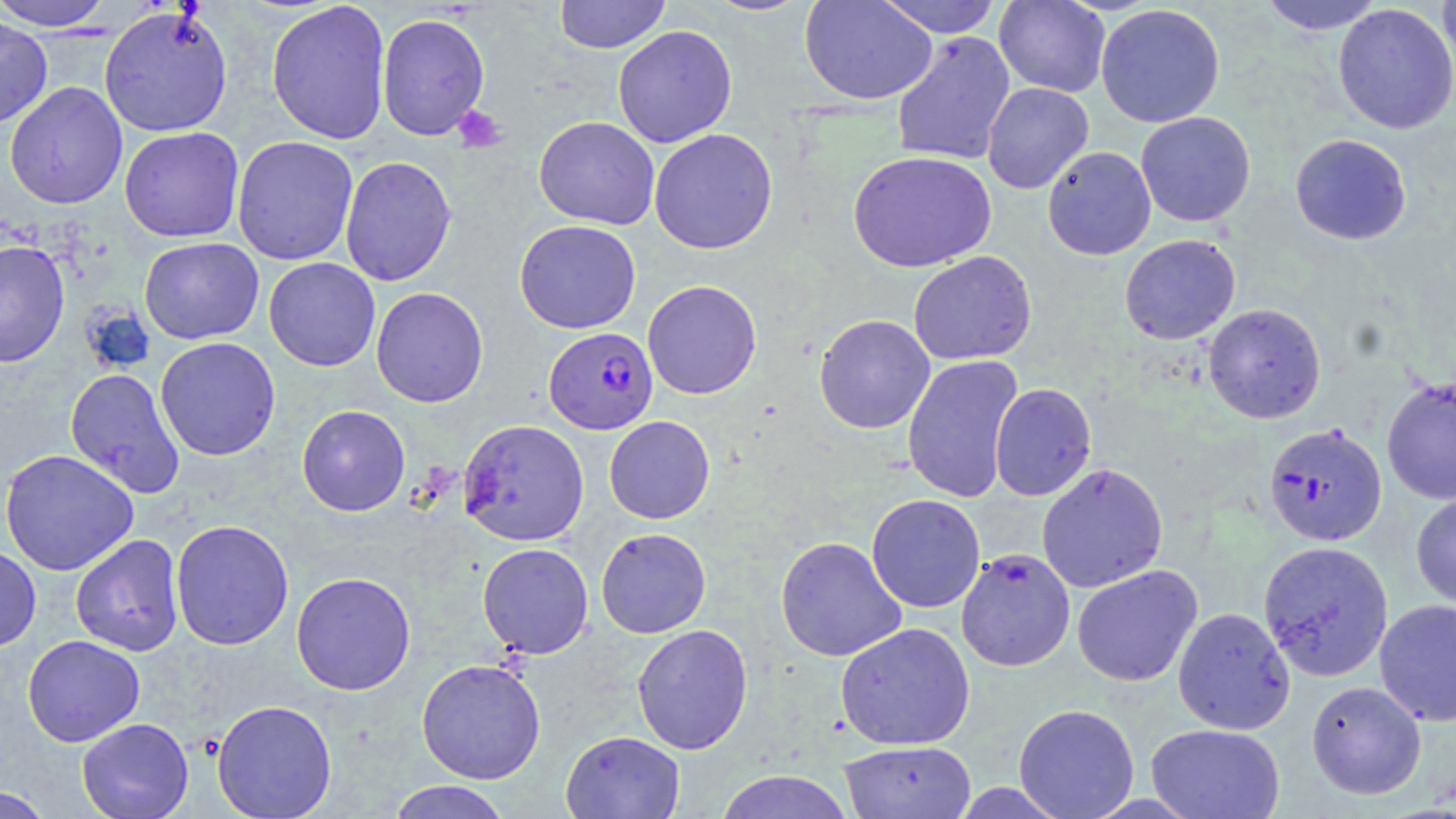

Summary:
  - Coordinate format: approximate bounding boxes as (x1, y1, x2, y2) in pixels
  - Uninfected red blood cell locations: (0, 0, 117, 31), (554, 0, 671, 54), (702, 0, 813, 17), (799, 0, 937, 105), (875, 0, 1003, 38), (994, 0, 1110, 97), (1257, 0, 1388, 35), (1437, 0, 1456, 83), (266, 1, 391, 144), (1333, 3, 1456, 135), (1096, 4, 1225, 128), (98, 5, 234, 138), (377, 12, 490, 141), (0, 15, 53, 129), (613, 24, 738, 148), (891, 31, 1016, 166), (4, 82, 128, 210), (982, 82, 1093, 194), (1136, 111, 1256, 227), (534, 116, 659, 230), (119, 127, 244, 242), (649, 128, 778, 254), (1290, 133, 1412, 245), (232, 135, 359, 266), (1042, 146, 1156, 260), (848, 151, 997, 272), (340, 155, 457, 287), (514, 220, 641, 334), (1119, 234, 1240, 344), (139, 237, 264, 344), (0, 240, 70, 368), (908, 251, 1037, 365), (264, 258, 380, 371), (642, 280, 762, 399), (371, 287, 488, 408), (1203, 303, 1326, 424), (814, 314, 935, 433), (155, 337, 281, 461), (902, 355, 1022, 504), (65, 368, 186, 498), (1381, 376, 1456, 505), (989, 383, 1097, 501), (297, 405, 411, 516), (604, 416, 715, 524), (458, 419, 590, 545), (0, 449, 139, 576), (1036, 462, 1168, 592), (1411, 491, 1456, 609), (866, 493, 985, 613), (170, 519, 294, 650), (596, 528, 711, 638), (70, 534, 184, 656), (775, 536, 907, 661), (1258, 540, 1394, 681), (477, 542, 594, 658), (0, 544, 41, 652), (956, 548, 1075, 672), (1072, 565, 1203, 687), (291, 571, 416, 695), (1375, 599, 1456, 726), (1173, 607, 1295, 734), (835, 622, 975, 750), (631, 624, 753, 754), (22, 635, 145, 747), (416, 658, 546, 784), (1306, 680, 1427, 799), (211, 699, 337, 818), (1013, 703, 1140, 819), (76, 717, 194, 819), (1146, 723, 1285, 819), (560, 730, 685, 819), (838, 740, 977, 819), (714, 770, 855, 819), (386, 781, 513, 819), (1, 784, 55, 819)
  - Platelet locations: (452, 105, 507, 153)
  - Plasmodium falciparum-infected red blood cell locations: (543, 327, 658, 434), (1263, 423, 1386, 546)
  - Slide-level diagnosis: Plasmodium falciparum
  - Modality: optical microscopy
  - Field of view: single
  - Stain: May-Grünwald-Giemsa
  - Magnification: 1000x
  - Preparation: thin blood smear
  - Image size: 1456×819 pixels